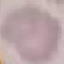 Malaria status: uninfected. Giemsa stain. Photographed with a smartphone camera at the microscope eyepiece. Thin blood film. Automatically extracted cell patch, resized to 64 × 64 pixels.